State the preparation type.
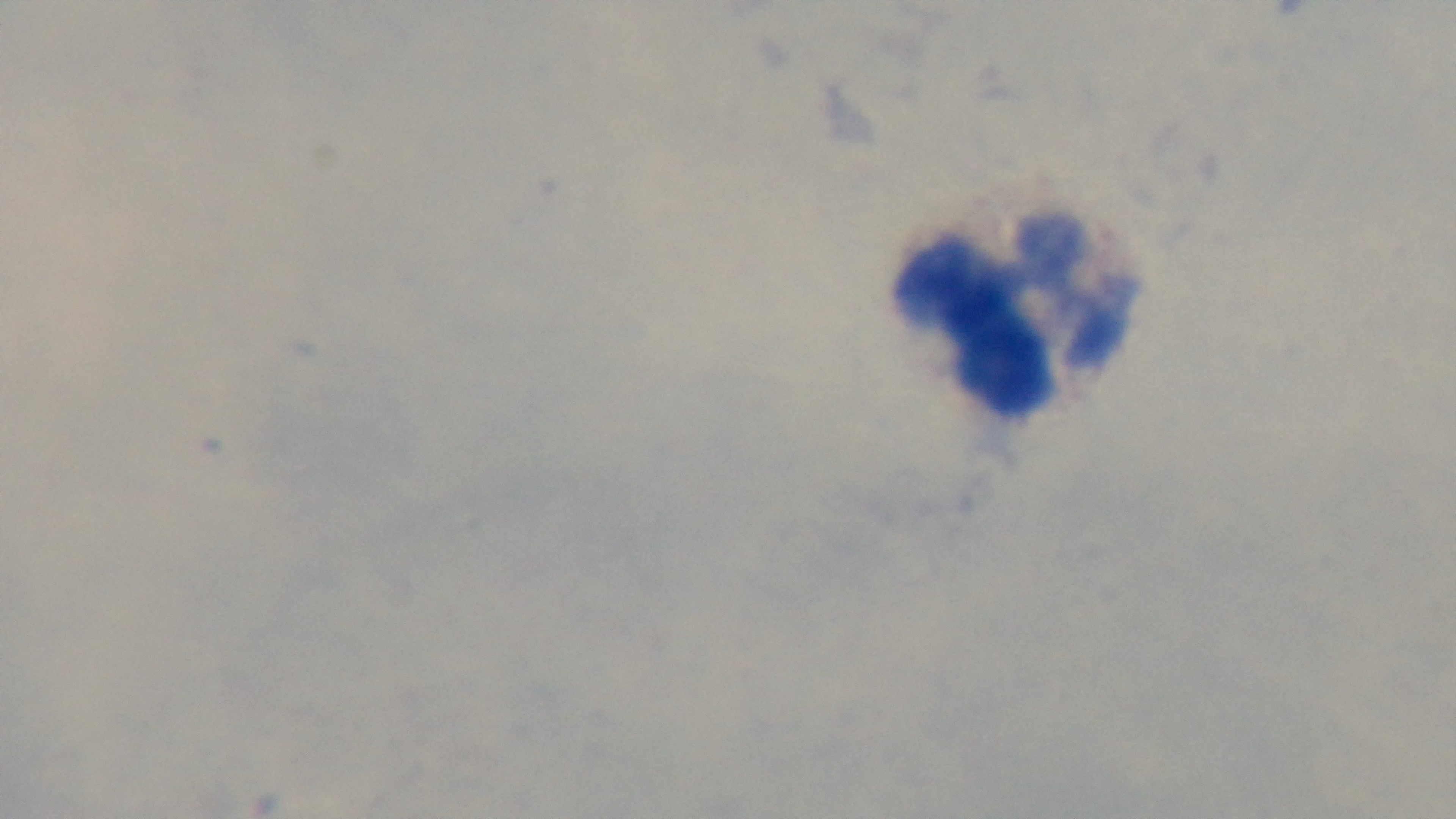
It is a thick blood film.

capture = mounted 4K digital camera
modality = light microscopy
objective = 100x oil immersion
malaria status = negative
stain = Giemsa
field of view = single